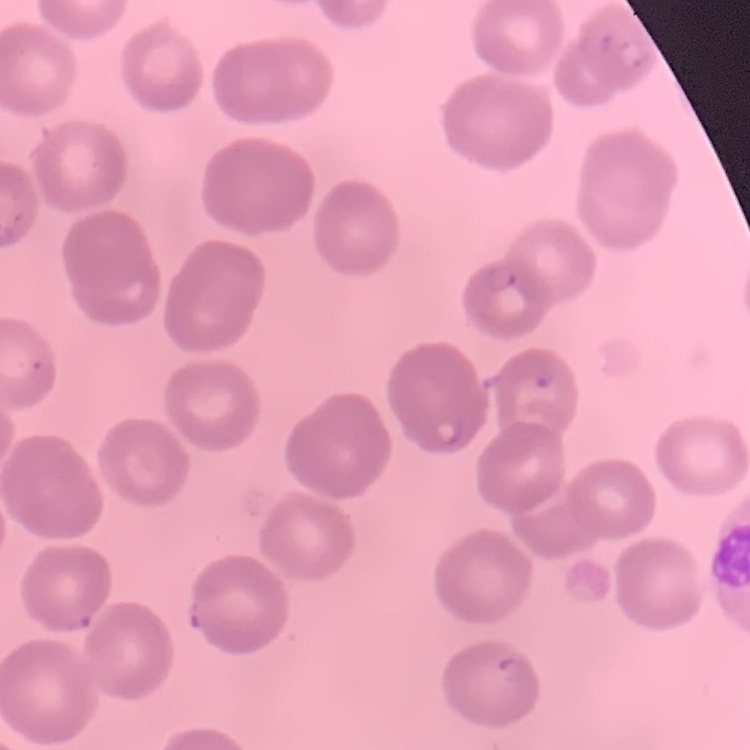

erythrocyte_morphology: no rouleaux formation
preparation: thin blood smear
stain: Field's or Giemsa
image_type: one tile cut from a larger photomicrograph